Locate every blood parasite and identify its species.
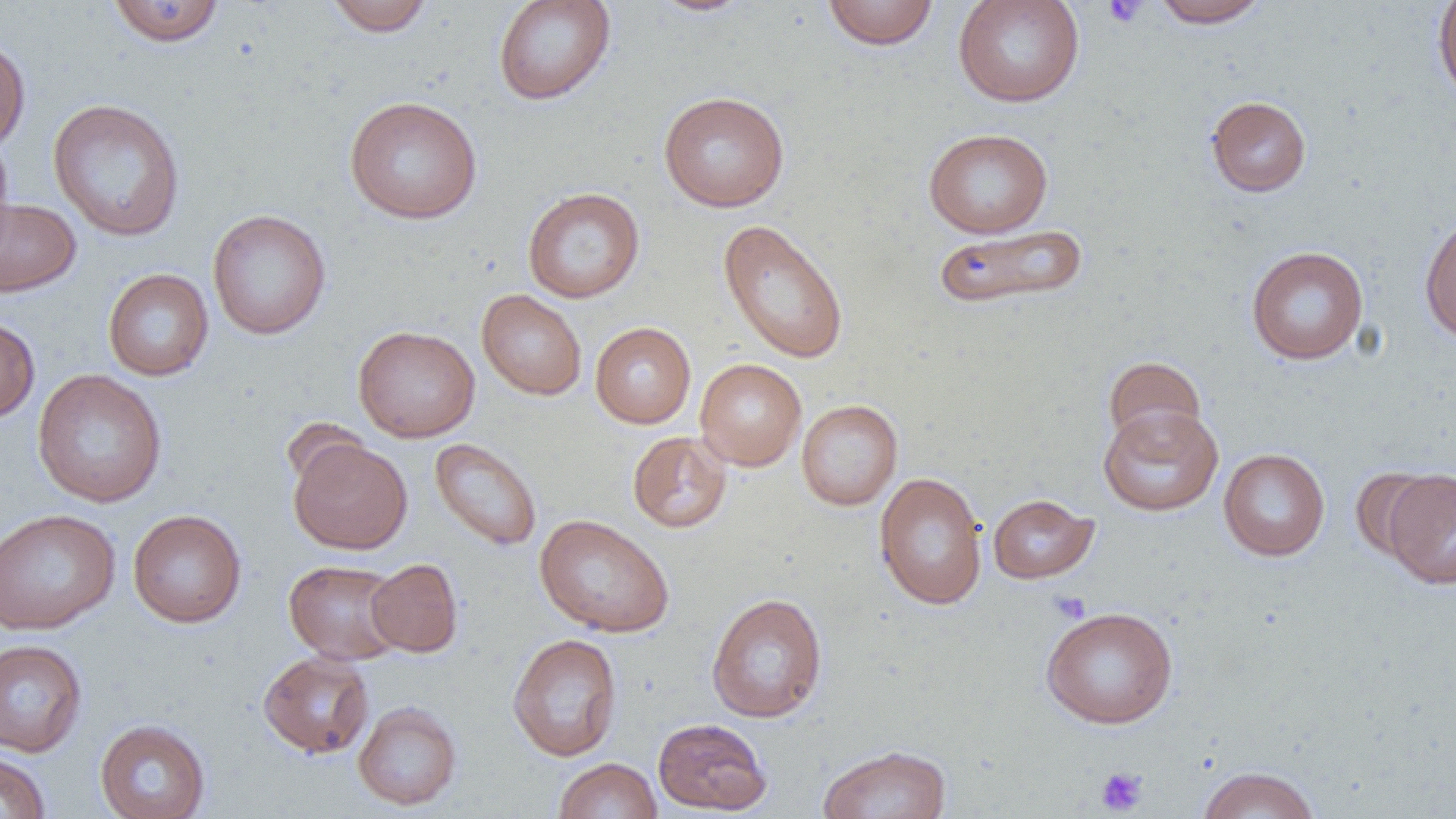

No blood parasites observed.

Approximate bounding boxes as (x1,y1)-(x2,y2) corner pairs in pixels. Uninfected red blood cell locations: (324,0)-(435,36), (492,0)-(616,106), (648,0)-(755,17), (952,0)-(1085,108), (1150,0)-(1272,28), (107,1)-(226,47), (821,1)-(940,50), (1432,1)-(1456,105), (0,34)-(31,155), (658,91)-(790,212), (1206,95)-(1312,197), (344,96)-(483,224), (47,98)-(186,242), (923,128)-(1053,238), (0,131)-(15,255), (523,187)-(645,303), (0,197)-(81,297), (207,209)-(331,340), (1419,212)-(1456,345), (718,218)-(850,364), (932,224)-(1091,311), (1246,245)-(1368,365), (102,268)-(214,381), (476,289)-(587,400), (0,315)-(40,424), (590,322)-(695,428), (353,324)-(480,442), (1103,356)-(1206,449), (694,358)-(807,471), (32,369)-(168,507), (796,399)-(903,510), (1097,404)-(1223,517), (627,431)-(732,533), (288,437)-(413,555), (429,438)-(542,551), (1218,448)-(1330,561), (1381,467)-(1456,590), (874,471)-(988,610), (987,493)-(1099,584), (0,509)-(120,635), (128,509)-(246,628), (534,513)-(674,637), (366,558)-(463,657), (283,560)-(405,665), (705,592)-(828,723), (1040,605)-(1178,728), (507,633)-(623,761), (0,639)-(88,757), (258,651)-(375,758), (353,700)-(462,810), (653,717)-(772,815), (95,718)-(210,819), (816,744)-(952,819), (0,751)-(51,819), (553,757)-(662,818), (1196,765)-(1321,819). Platelet locations: (1102,0)-(1149,28), (1047,590)-(1092,624), (1095,767)-(1148,815). Slide-level diagnosis: no evidence of blood parasites. Image is 1456×819 pixels. One field of a larger specimen. Captured at 1000x magnification. Light microscopy. Thin blood smear.